Report the malaria status of this cell.
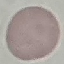
Uninfected.

Acquired by smartphone through the microscope eyepiece. Giemsa-stained preparation. Automatically extracted cell patch, resized to 64 × 64 pixels. Thin blood smear.